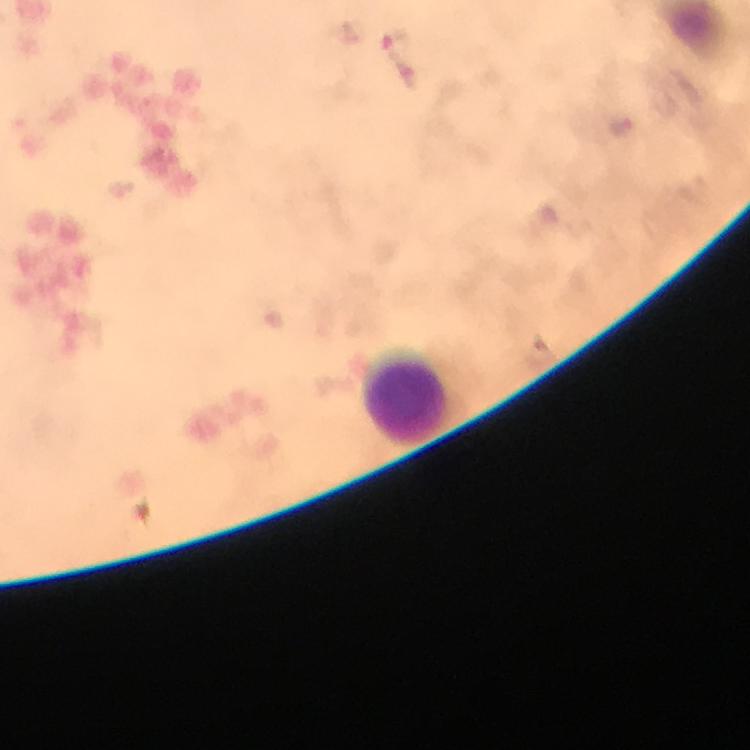 Approximate centers as [x, y] in pixels. Leukocyte locations: [408, 397]. Malaria parasite locations: [397, 44]. Giemsa stain. Image is 750×750 pixels. From a diagnostic examination for malaria. A crop from one field of view. 100x magnification. Thick blood smear. Smartphone photograph taken through a microscope. Immersion oil applied.